State the blood parasite species.
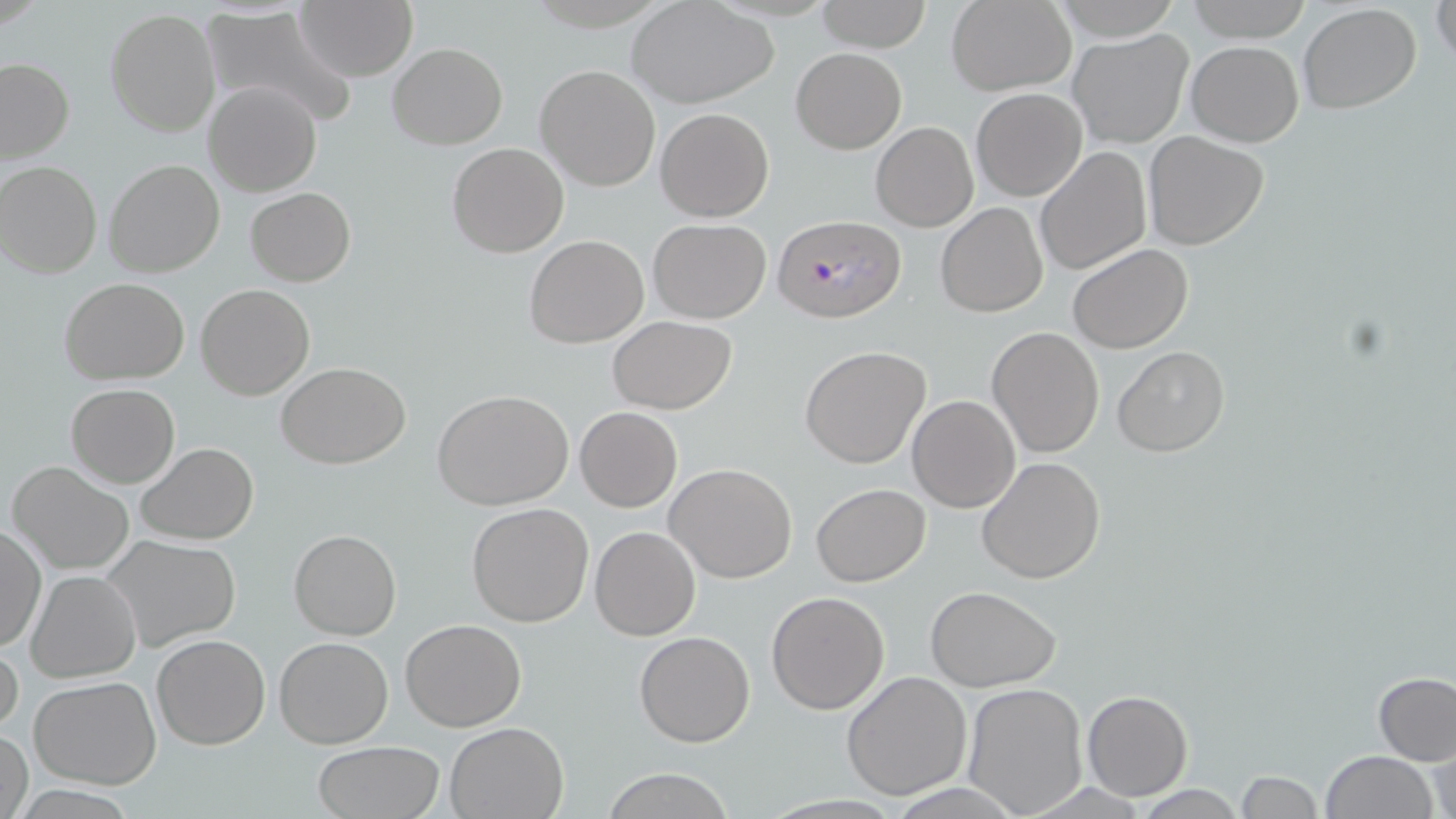

Plasmodium falciparum.

Summary:
  - Coordinate format: approximate bounding boxes as [x1, y1, x2, y2] in pixels
  - Uninfected red blood cell locations: [815, 0, 930, 51], [1052, 0, 1182, 40], [1184, 0, 1314, 43], [1430, 0, 1454, 69], [628, 1, 779, 109], [945, 1, 1077, 96], [296, 2, 417, 81], [1297, 4, 1422, 114], [201, 5, 357, 130], [105, 8, 220, 138], [1067, 29, 1194, 149], [1185, 40, 1305, 148], [387, 43, 508, 148], [789, 47, 906, 153], [0, 57, 74, 165], [534, 64, 661, 191], [202, 81, 322, 198], [971, 87, 1087, 201], [655, 108, 774, 223], [871, 121, 978, 232], [1142, 130, 1270, 251], [446, 143, 569, 258], [1034, 145, 1152, 277], [104, 159, 226, 279], [0, 161, 102, 279], [245, 186, 356, 287], [935, 203, 1049, 317], [648, 218, 772, 323], [525, 235, 648, 349], [1067, 243, 1193, 353], [59, 277, 189, 384], [196, 283, 315, 400], [609, 316, 736, 414], [987, 327, 1105, 460], [799, 345, 931, 469], [1112, 345, 1229, 457], [278, 362, 410, 468], [66, 382, 180, 487], [431, 390, 575, 511], [906, 395, 1021, 513], [574, 407, 682, 512], [136, 443, 257, 545], [976, 456, 1105, 585], [7, 461, 134, 575], [666, 462, 799, 584], [810, 483, 930, 585], [467, 502, 596, 627], [0, 523, 46, 655], [590, 526, 701, 641], [288, 530, 402, 641], [101, 535, 242, 651], [25, 569, 142, 682], [925, 586, 1061, 692], [768, 591, 890, 712], [400, 619, 527, 732], [634, 631, 756, 747], [152, 634, 270, 749], [274, 635, 393, 748], [0, 638, 24, 739], [840, 670, 972, 800], [1373, 672, 1456, 765], [29, 676, 161, 790], [961, 683, 1089, 817], [1081, 690, 1193, 801], [444, 722, 568, 818], [0, 725, 32, 819], [1426, 736, 1454, 819], [312, 741, 444, 819], [1319, 750, 1439, 819], [600, 769, 736, 819], [1234, 771, 1326, 818], [1130, 785, 1252, 818]
  - Plasmodium falciparum-infected red blood cell locations: [774, 214, 908, 324]
  - Field of view: single
  - Image size: 1456×819 pixels
  - Magnification: 1000x
  - Stain: May-Grünwald-Giemsa
  - Modality: light microscopy
  - Preparation: thin blood smear